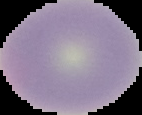
Summary:
  - Image size: 142×115 pixels
  - Preparation: thin blood film
  - Result: negative for Plasmodium parasites
  - Image type: cell region segmented out of the field of view; surrounding area masked to black